Comment on the morphology of the erythrocytes.
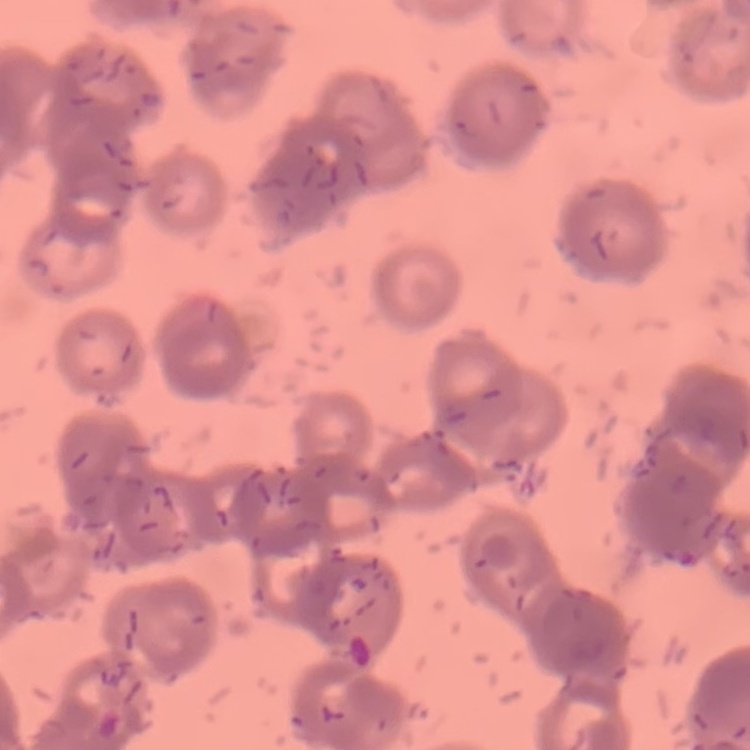

They show rouleaux formation.

image_type: square crop of a larger photomicrograph
stain: Field's or Giemsa
preparation: thin blood film